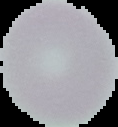
Summary:
  - Image type: cell region segmented out of the field of view; surrounding area masked to black
  - Result: no Plasmodium parasites seen
  - Preparation: thin blood film
  - Image size: 118×127 pixels